Mark where platelets are.
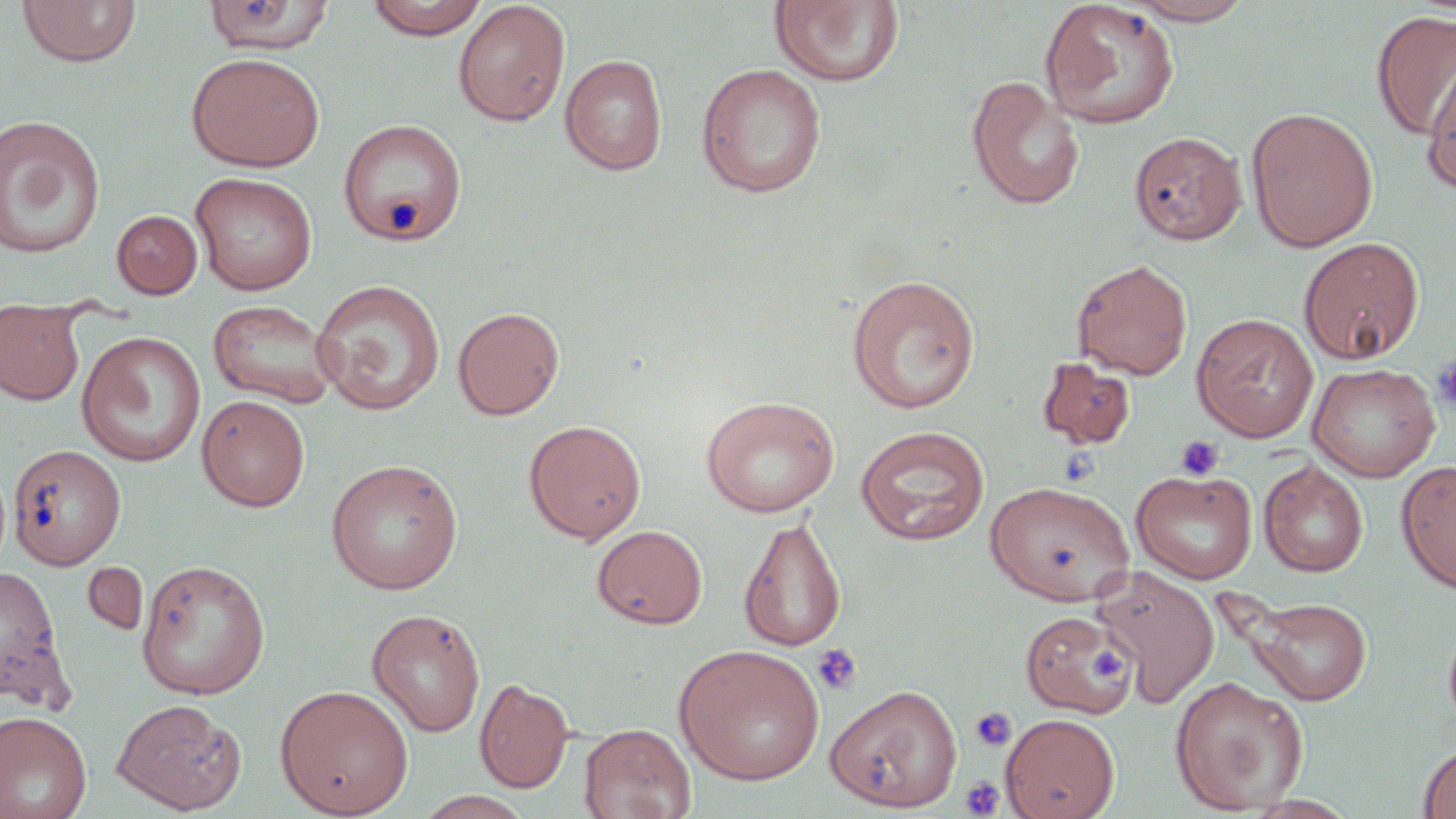
Approximate bounding boxes as (x1,y1)-(x2,y2) corner pairs in pixels.
Platelets: (1432,354)-(1456,415), (1175,435)-(1226,482), (812,643)-(862,695), (1089,646)-(1131,683), (970,707)-(1017,752), (960,775)-(1005,817).

Uninfected red blood cell locations: (203,0)-(335,56), (365,0)-(489,39), (1039,0)-(1180,129), (1122,0)-(1257,25), (16,1)-(142,68), (452,1)-(571,127), (770,1)-(905,87), (1371,9)-(1456,140), (186,51)-(325,172), (559,54)-(668,175), (1421,56)-(1456,195), (696,63)-(827,199), (966,74)-(1085,210), (1246,106)-(1379,252), (0,115)-(106,259), (338,118)-(467,246), (1129,131)-(1246,245), (190,171)-(317,296), (112,210)-(202,299), (1298,236)-(1424,364), (1071,259)-(1193,379), (845,273)-(981,414), (311,279)-(446,416), (0,298)-(86,406), (208,300)-(336,408), (452,306)-(565,420), (1191,313)-(1319,442), (76,331)-(207,467), (1037,356)-(1136,449), (1308,362)-(1440,481), (196,395)-(310,512), (700,395)-(840,517), (523,419)-(646,544), (855,426)-(990,546), (7,444)-(126,570), (325,458)-(464,594), (1259,460)-(1368,577), (1396,460)-(1456,594), (1131,468)-(1258,585), (985,480)-(1135,606), (738,515)-(848,653), (591,524)-(708,629), (136,558)-(271,700), (81,561)-(149,637), (0,564)-(71,709), (1091,565)-(1220,709), (1244,596)-(1372,705), (367,608)-(486,737), (1020,609)-(1136,718), (674,645)-(826,786), (1169,675)-(1309,815), (475,677)-(574,793), (825,683)-(963,812), (274,685)-(414,818), (111,698)-(246,814), (0,710)-(92,819), (1001,713)-(1120,819), (579,723)-(696,819), (1417,743)-(1456,819), (414,791)-(535,819). Slide-level diagnosis: no evidence of blood parasites. Single field of view. Thin blood smear. Optical microscopy. 1000x magnification. Image is 1456×819 pixels. May-Grünwald-Giemsa-stained preparation.